Identify the parasite.
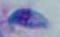
Toxoplasma gondii.

Photomicrograph. Captured at 1000x magnification.